Assess the morphology of the erythrocytes.
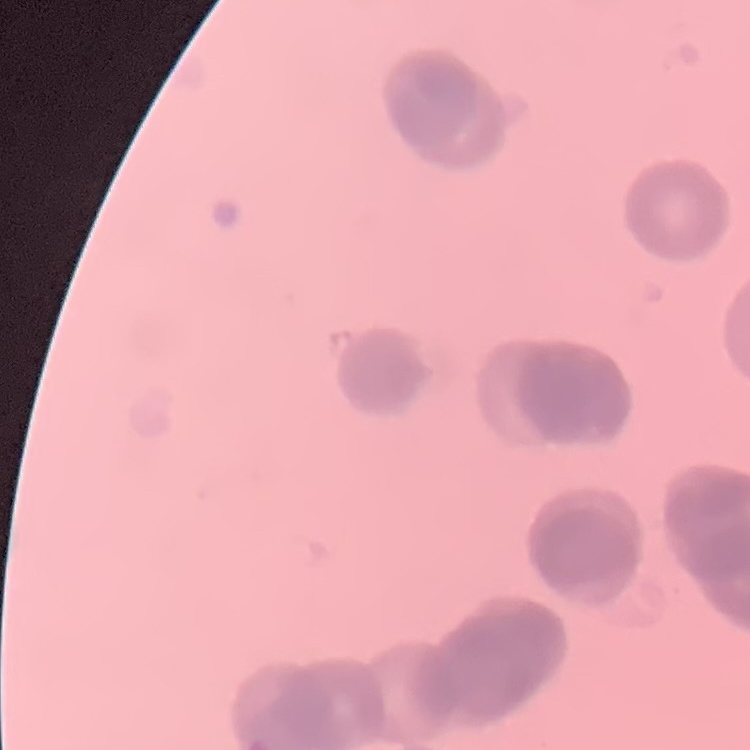
They show rouleaux formation.

Summary:
  - Preparation: thin peripheral smear
  - Stain: Field's or Giemsa
  - Image type: one tile cut from a larger photomicrograph